Draw a bounding box around every malaria parasite, every leukocyte, and every artifact (stain precipitate or debris).
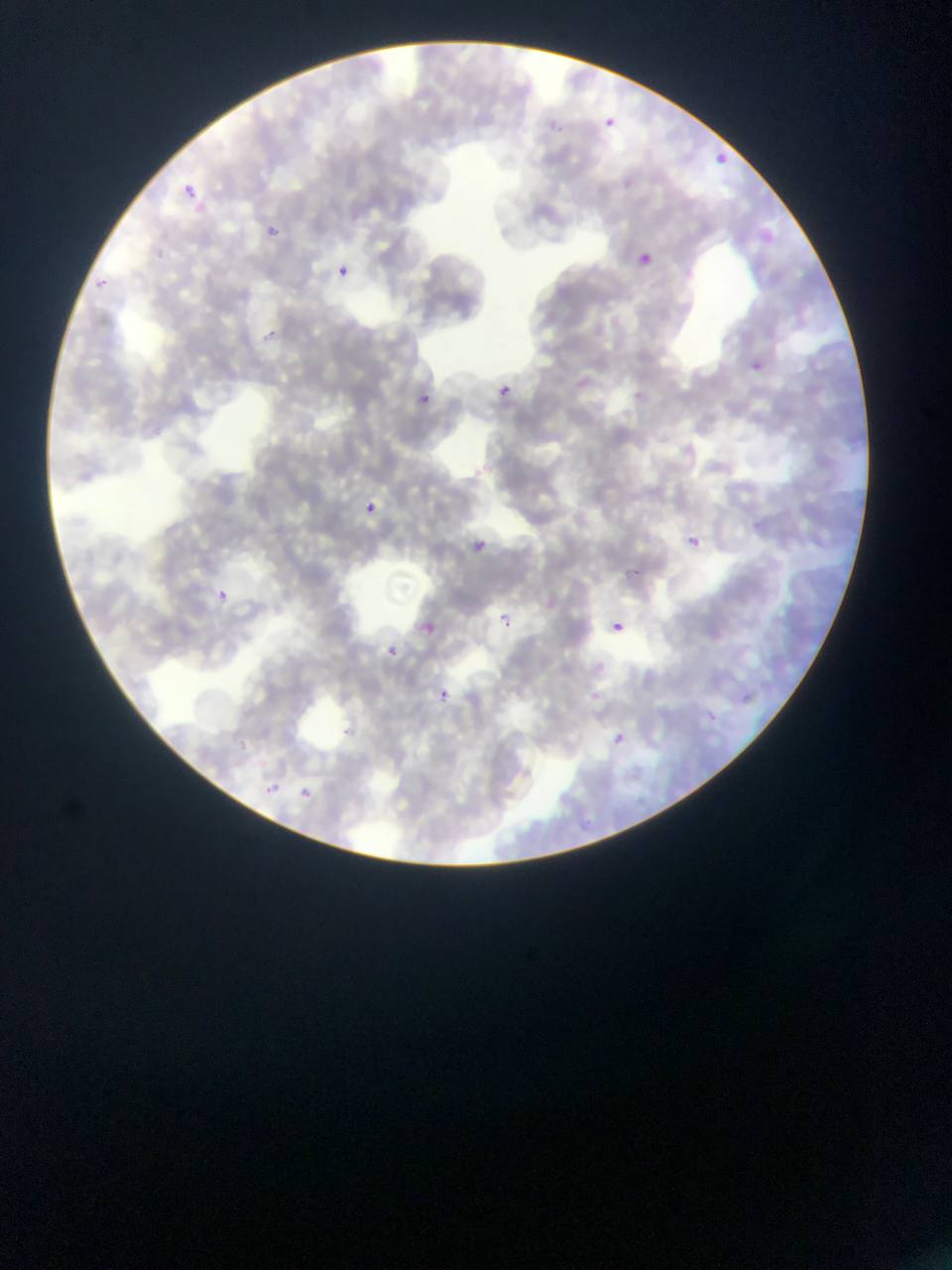
Approximate bounding boxes as [left, top, right, bottom] in pixels.
Malaria parasites: [595, 114, 622, 136], [710, 147, 732, 169], [181, 182, 200, 200], [269, 220, 285, 235], [634, 252, 653, 267], [335, 266, 351, 280], [97, 277, 119, 290], [260, 328, 281, 338], [752, 360, 766, 378], [501, 381, 532, 398], [413, 390, 436, 410], [355, 498, 380, 518], [463, 535, 495, 563], [687, 536, 700, 548], [627, 566, 648, 578], [211, 588, 232, 606], [491, 611, 517, 634], [416, 619, 440, 640], [606, 622, 622, 639], [611, 622, 622, 632], [380, 643, 401, 662], [430, 685, 455, 706], [587, 689, 603, 705], [606, 730, 629, 749], [251, 756, 272, 775], [257, 779, 281, 801], [295, 782, 319, 804].
No leukocytes observed.

Image is 952×1270 pixels. Thin blood smear. Photographed through a microscope with a mobile-phone camera. Sample from Ghana. Single field of view.